Describe the morphology of the erythrocytes.
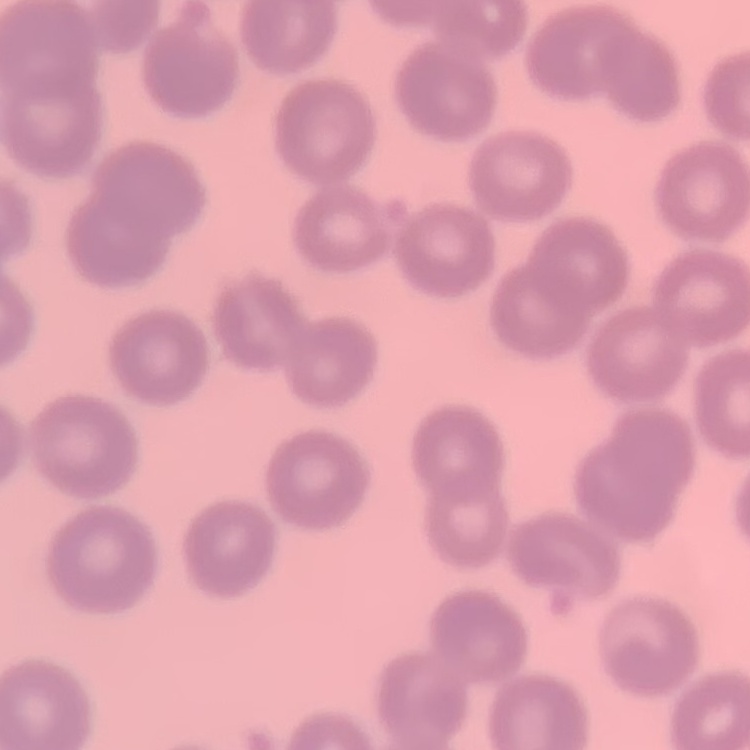
They show no rouleaux formation.

Thin peripheral smear. Stained with either Field's or Giemsa. One tile cut from a larger photomicrograph.